Assess this cell for malaria.
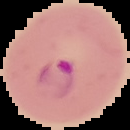
Parasitized.

Summary:
  - Image type: segmented cell region with the area outside set to black
  - Image size: 130×130 pixels
  - Preparation: thin blood smear